Find each cell and give its type.
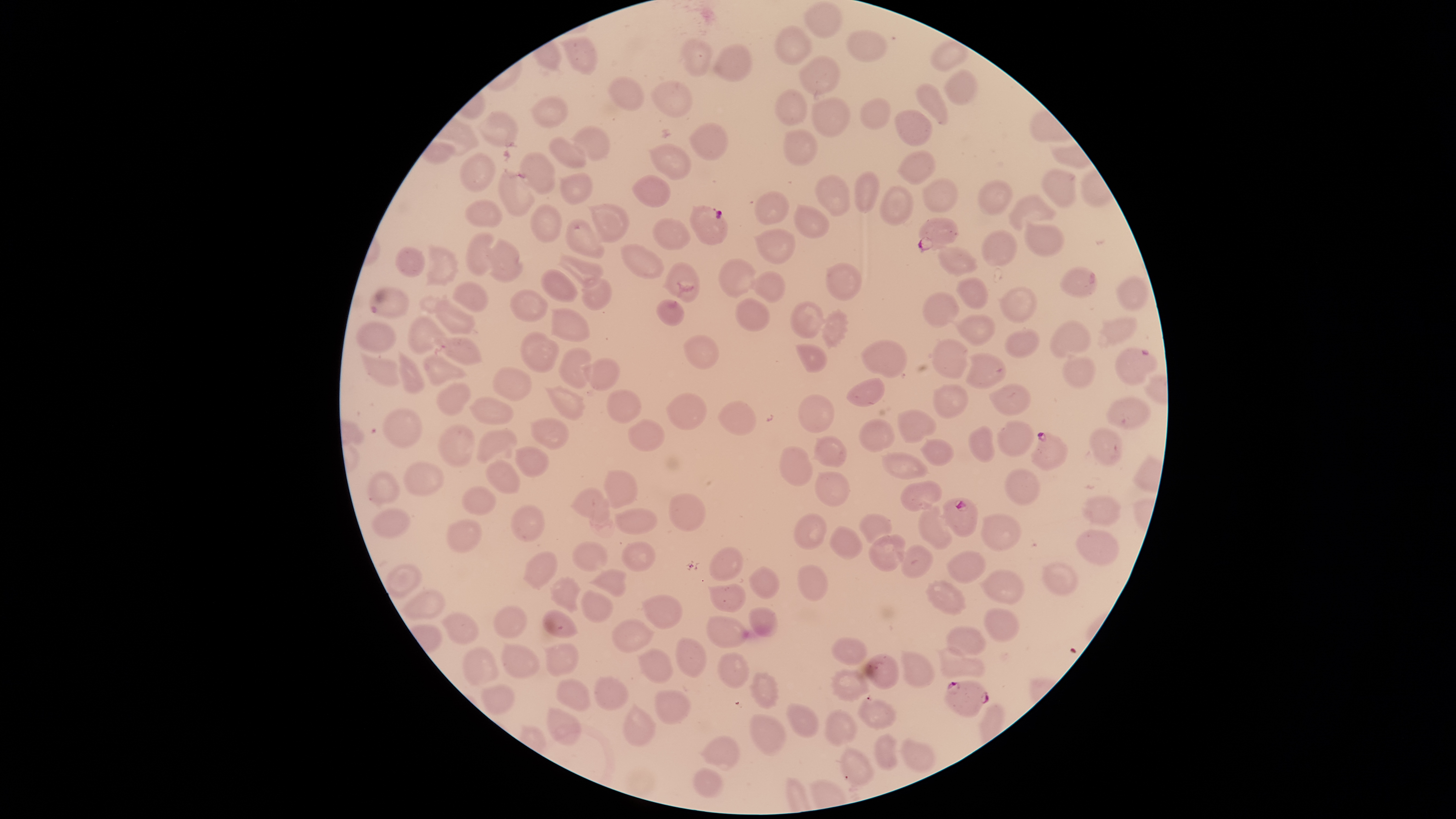
Approximate bounding boxes as (left, top, right, bottom) in pixels.
Parasitized RBCs: (690, 205, 729, 246), (918, 217, 960, 253), (1116, 347, 1158, 385), (1030, 432, 1068, 472), (940, 497, 979, 538), (944, 680, 990, 719).
Uninfected RBCs: (803, 0, 842, 39), (774, 24, 811, 65), (846, 29, 888, 62), (558, 37, 598, 75), (681, 38, 712, 77), (930, 39, 971, 73), (712, 42, 752, 83), (799, 55, 841, 95), (943, 68, 979, 104), (607, 76, 644, 111), (648, 81, 694, 117), (914, 82, 950, 125), (773, 88, 807, 127), (529, 95, 569, 128), (809, 96, 851, 138), (860, 96, 891, 130), (894, 108, 933, 147), (475, 109, 519, 148), (689, 122, 729, 160), (571, 125, 611, 160), (784, 128, 819, 166), (549, 135, 587, 170), (648, 143, 692, 181), (896, 150, 936, 185), (519, 151, 557, 194), (457, 153, 497, 193), (1040, 168, 1078, 208), (854, 170, 880, 213), (497, 171, 536, 216), (556, 172, 593, 206), (814, 174, 850, 216), (631, 175, 670, 208), (922, 177, 959, 211), (976, 178, 1012, 216), (879, 184, 914, 225), (754, 189, 791, 226), (1008, 195, 1055, 230), (464, 199, 503, 226), (587, 202, 630, 244), (529, 203, 564, 243), (793, 203, 830, 240), (651, 216, 691, 250), (565, 218, 605, 258), (1025, 218, 1065, 258), (752, 226, 796, 264), (981, 229, 1017, 267), (464, 230, 500, 276), (487, 237, 524, 283), (425, 242, 459, 287), (620, 243, 665, 280), (394, 245, 425, 277), (936, 245, 979, 276), (555, 251, 604, 289), (718, 257, 756, 299), (662, 261, 700, 303), (825, 262, 862, 301), (1059, 266, 1097, 297), (539, 267, 579, 303), (749, 271, 786, 304), (1115, 273, 1150, 312), (955, 276, 989, 309), (580, 277, 612, 311), (451, 281, 489, 313), (999, 285, 1037, 322), (368, 286, 410, 319), (509, 288, 548, 322), (920, 291, 960, 328), (735, 297, 770, 331), (656, 299, 685, 326), (433, 300, 475, 336), (790, 301, 826, 339), (548, 307, 591, 342), (821, 308, 850, 350), (948, 313, 996, 347), (405, 314, 449, 354), (1097, 316, 1139, 348), (1049, 320, 1091, 358), (356, 321, 396, 353), (1004, 327, 1041, 358), (519, 330, 559, 373), (682, 334, 721, 370), (434, 336, 483, 367), (932, 338, 969, 379), (860, 339, 908, 378), (794, 343, 828, 373), (557, 347, 592, 388), (397, 349, 425, 395), (1061, 350, 1099, 388), (964, 351, 1008, 390), (360, 352, 403, 385), (422, 354, 469, 387), (579, 358, 620, 392), (492, 365, 533, 402), (846, 378, 886, 407), (435, 381, 473, 416), (988, 382, 1031, 417), (931, 383, 971, 418), (542, 385, 586, 420), (606, 388, 642, 424), (665, 393, 707, 430), (798, 394, 835, 434), (468, 395, 514, 425), (1104, 395, 1151, 429), (717, 399, 757, 435), (382, 407, 422, 448), (896, 408, 937, 443), (529, 416, 570, 450), (858, 418, 895, 453), (628, 419, 666, 452), (997, 419, 1035, 457), (438, 424, 475, 469), (967, 424, 996, 464), (475, 426, 518, 465), (1089, 426, 1125, 467), (811, 435, 848, 468), (918, 437, 956, 466), (514, 445, 549, 479), (779, 445, 813, 486), (881, 451, 928, 480), (484, 459, 521, 495), (402, 461, 446, 497), (602, 468, 639, 509), (1004, 468, 1041, 506), (366, 469, 400, 505), (813, 471, 851, 508), (900, 479, 943, 512), (461, 485, 497, 515), (570, 488, 610, 525), (668, 492, 707, 531), (1081, 495, 1123, 525), (510, 504, 546, 543), (918, 506, 953, 550), (614, 507, 658, 535), (370, 509, 411, 539), (980, 512, 1022, 552), (793, 513, 827, 550), (858, 513, 892, 543), (446, 519, 483, 555), (829, 524, 863, 561), (1075, 528, 1120, 566), (869, 532, 906, 572), (571, 540, 609, 573), (621, 541, 656, 572), (896, 544, 933, 578), (709, 546, 744, 581), (523, 551, 559, 591), (946, 551, 988, 584), (1041, 561, 1080, 596), (383, 563, 423, 598), (797, 563, 829, 602), (747, 565, 779, 598), (589, 568, 627, 597), (979, 569, 1025, 605), (549, 575, 581, 613), (924, 579, 967, 616), (706, 584, 746, 612), (580, 589, 615, 622), (401, 590, 447, 621), (641, 592, 684, 631), (493, 604, 527, 638), (748, 607, 777, 637), (983, 607, 1020, 643), (541, 609, 579, 638), (440, 612, 480, 645), (706, 616, 749, 648), (611, 618, 655, 654), (945, 625, 987, 658), (675, 636, 708, 679), (831, 637, 868, 666), (501, 641, 541, 680), (541, 642, 580, 676), (936, 644, 986, 679), (462, 647, 500, 686), (636, 647, 673, 684), (899, 649, 936, 689), (718, 650, 750, 689), (864, 652, 900, 690), (831, 668, 872, 703), (748, 671, 781, 709), (593, 675, 629, 711), (555, 677, 592, 712), (480, 683, 516, 716), (654, 688, 691, 725), (856, 695, 898, 730), (621, 702, 658, 747), (785, 702, 821, 738), (546, 706, 582, 746), (824, 708, 859, 747), (748, 713, 787, 755), (874, 733, 897, 770), (698, 735, 740, 771), (898, 737, 936, 773), (840, 745, 877, 786), (691, 766, 722, 797).
No WBCs identified.

Giemsa stain. Single field of view. Image is 1456×819 pixels. The visible region is circular. Species: Plasmodium falciparum. Thin blood film. Photographed with a smartphone camera through the microscope eyepiece.